Locate and identify every blood parasite.
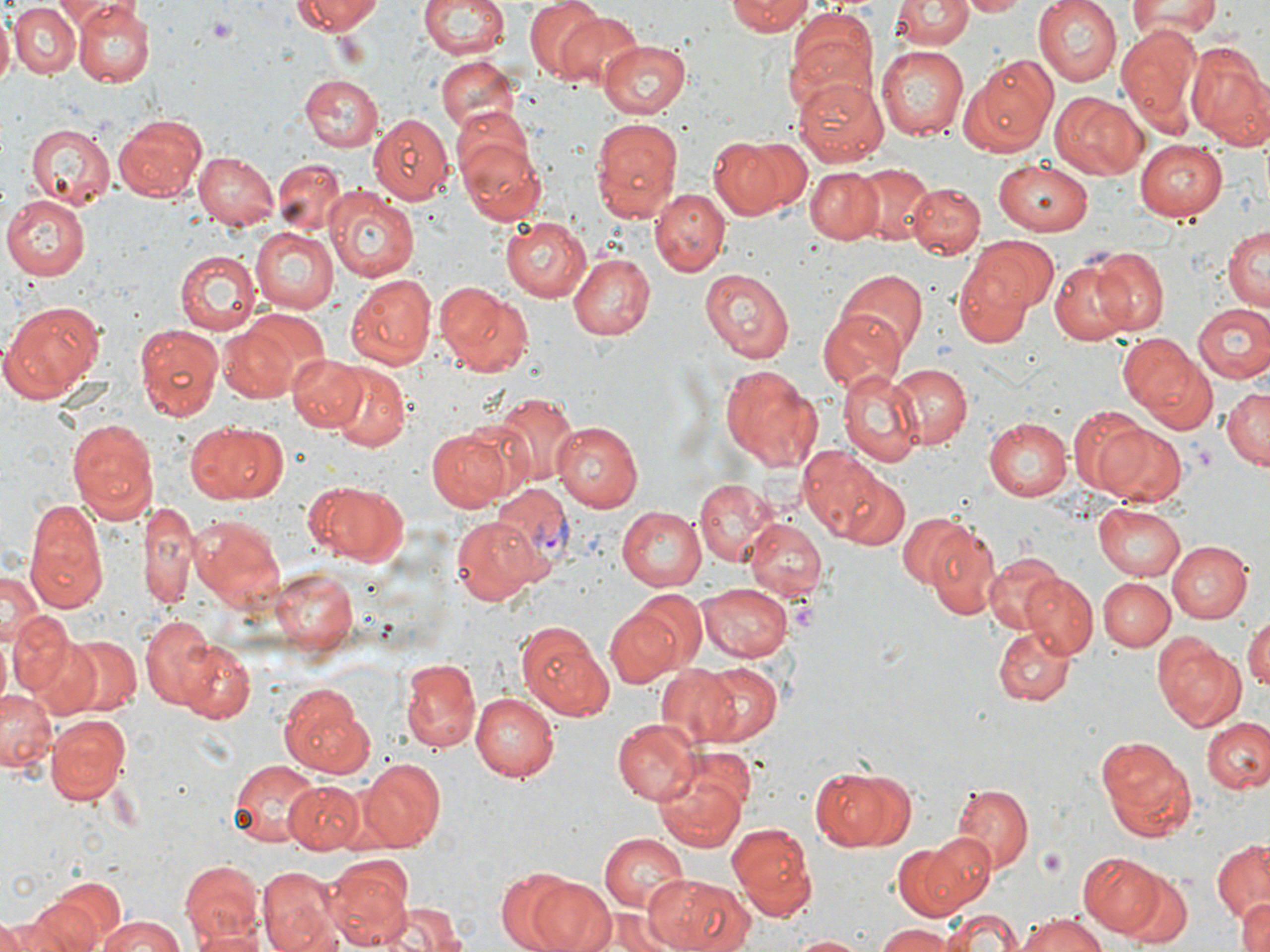
Approximate bounding boxes as (x1, y1, x2, y2) in pixels.
Plasmodium vivax-infected red blood cells: (488, 484, 572, 575).
No Plasmodium falciparum, Plasmodium ovale, Plasmodium malariae, Babesia divergens, or Trypanosoma brucei observed.

slide_level_diagnosis: Plasmodium vivax
field_of_view: single
preparation: thin blood smear
image_size: 1270×952 pixels
magnification: 1000x
stain: May-Grünwald-Giemsa
uninfected_red_blood_cell_locations: 'approximate bounding boxes as (x1, y1, x2, y2) in pixels: (54, 0, 119, 24), (292, 0, 384, 36), (417, 0, 510, 62), (525, 0, 608, 82), (725, 0, 814, 36), (894, 0, 970, 51), (961, 0, 1029, 17), (1035, 0, 1124, 86), (1127, 0, 1225, 42), (9, 3, 79, 77), (74, 3, 153, 85), (784, 10, 879, 109), (0, 11, 13, 87), (552, 12, 646, 96), (1117, 26, 1203, 123), (598, 41, 691, 119), (1187, 43, 1270, 144), (877, 45, 968, 138), (432, 53, 524, 140), (965, 55, 1057, 152), (299, 72, 383, 151), (796, 74, 890, 166), (1054, 93, 1148, 179), (114, 112, 208, 204), (370, 114, 452, 207), (450, 115, 547, 223), (589, 115, 685, 222), (25, 122, 116, 213), (706, 134, 806, 221), (1134, 140, 1228, 224), (192, 151, 278, 230), (993, 159, 1093, 233), (273, 160, 345, 234), (852, 165, 932, 247), (805, 168, 885, 244), (905, 182, 984, 259), (324, 187, 421, 283), (650, 188, 728, 277), (3, 195, 91, 279), (500, 216, 592, 301), (1224, 225, 1269, 310), (248, 227, 337, 311), (950, 238, 1056, 346), (175, 248, 259, 334), (1094, 248, 1168, 336), (567, 251, 654, 340), (1049, 256, 1143, 344), (701, 266, 792, 362), (838, 270, 926, 358), (345, 273, 436, 369), (433, 283, 532, 377), (0, 299, 106, 400), (1192, 303, 1270, 384), (819, 310, 903, 393), (217, 319, 305, 404), (133, 324, 227, 424), (1117, 333, 1217, 431), (287, 353, 367, 432), (886, 362, 972, 450), (327, 364, 410, 452), (717, 364, 822, 471), (837, 368, 923, 468), (1221, 383, 1270, 469), (490, 392, 580, 489), (1064, 414, 1156, 503), (64, 416, 157, 524), (983, 417, 1073, 502), (185, 420, 289, 507), (551, 421, 644, 512), (1095, 423, 1187, 507), (424, 425, 518, 512), (796, 445, 895, 544), (835, 470, 911, 552), (693, 476, 783, 566), (306, 480, 410, 567), (25, 499, 109, 612), (140, 499, 200, 610), (1094, 501, 1188, 582), (616, 505, 706, 591), (899, 511, 974, 588), (190, 514, 285, 608), (448, 517, 544, 605), (743, 518, 826, 604), (926, 526, 1002, 620), (1167, 539, 1253, 622), (983, 555, 1065, 636), (272, 565, 359, 652), (0, 566, 42, 654), (1024, 574, 1097, 656), (1098, 577, 1176, 650), (699, 580, 795, 661), (627, 590, 706, 674), (603, 607, 684, 689), (9, 609, 74, 698), (1245, 614, 1270, 692), (141, 615, 221, 710), (514, 619, 612, 720), (993, 626, 1073, 706), (1151, 632, 1248, 732), (63, 634, 143, 717), (27, 637, 107, 718), (181, 643, 255, 723), (399, 656, 482, 753), (695, 663, 782, 744), (657, 666, 738, 745), (277, 683, 374, 779), (0, 686, 55, 774), (471, 691, 559, 781), (45, 713, 130, 804), (611, 719, 701, 804), (1204, 719, 1270, 793), (1095, 736, 1197, 841), (651, 750, 754, 852), (227, 758, 318, 847), (360, 758, 446, 850), (809, 765, 912, 852), (285, 781, 364, 851), (951, 784, 1033, 872), (726, 822, 818, 916), (597, 833, 690, 912), (890, 837, 982, 918), (1212, 841, 1270, 923), (1078, 853, 1161, 934), (327, 855, 414, 950), (180, 858, 262, 945), (256, 866, 343, 952), (492, 869, 584, 951), (1113, 872, 1192, 949), (642, 875, 753, 952), (525, 877, 615, 952), (35, 880, 124, 950), (1233, 896, 1270, 952), (14, 899, 100, 952), (377, 901, 466, 952), (943, 908, 1022, 951), (590, 912, 680, 952), (1015, 912, 1109, 952), (2, 913, 68, 951), (92, 915, 190, 952), (872, 924, 958, 951), (1, 925, 27, 952), (189, 928, 269, 952), (790, 934, 870, 951)'
platelet_locations: 'approximate bounding boxes as (x1, y1, x2, y2) in pixels: (206, 14, 236, 45), (1038, 848, 1066, 877)'
modality: light microscopy